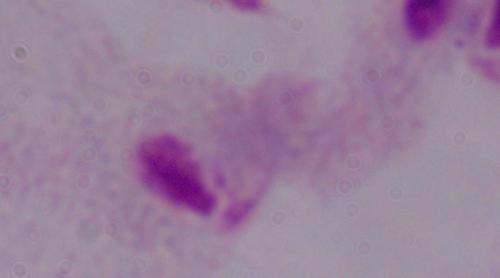 A trichomonad is seen. Micrograph. 1000x magnification.